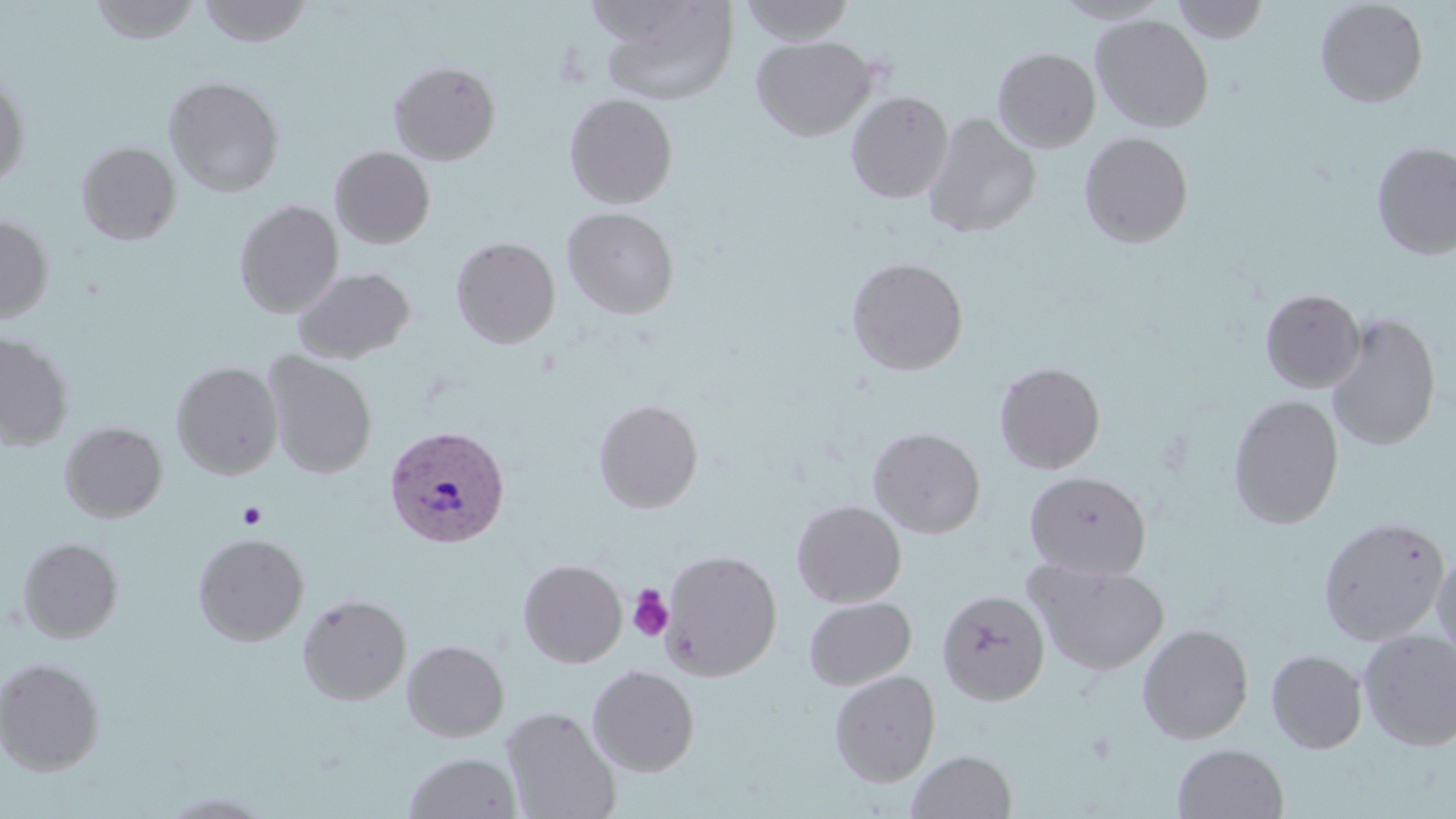

Summary:
  - Coordinate format: approximate bounding boxes as (x1, y1, x2, y2) in pixels
  - Platelet locations: (238, 501, 268, 528), (627, 584, 675, 642)
  - Plasmodium vivax-infected red blood cell locations: (383, 425, 511, 548)
  - Uninfected red blood cell locations: (89, 0, 202, 44), (198, 0, 313, 47), (739, 0, 857, 45), (1052, 0, 1173, 24), (1170, 0, 1271, 43), (1314, 0, 1428, 107), (593, 1, 739, 105), (1091, 14, 1214, 132), (751, 36, 878, 141), (992, 47, 1101, 153), (388, 60, 501, 165), (0, 74, 31, 192), (164, 76, 285, 197), (846, 91, 954, 203), (564, 92, 678, 209), (923, 112, 1042, 240), (1079, 131, 1194, 248), (76, 141, 181, 245), (1371, 141, 1456, 260), (329, 146, 435, 249), (234, 199, 344, 317), (562, 206, 680, 318), (0, 214, 54, 323), (450, 236, 561, 348), (846, 256, 968, 375), (291, 266, 416, 364), (1260, 288, 1367, 392), (1325, 312, 1442, 451), (0, 333, 75, 451), (263, 350, 378, 479), (171, 361, 284, 479), (994, 361, 1105, 474), (1228, 394, 1344, 529), (593, 398, 704, 513), (59, 421, 168, 523), (867, 426, 986, 538), (1024, 470, 1151, 579), (791, 499, 906, 608), (1317, 515, 1450, 646), (192, 532, 309, 646), (17, 536, 124, 642), (1431, 548, 1456, 669), (661, 549, 783, 680), (518, 558, 627, 668), (1024, 558, 1170, 676), (936, 589, 1049, 705), (298, 593, 412, 705), (804, 597, 917, 690), (1137, 624, 1254, 744), (1357, 629, 1456, 750), (402, 639, 510, 742), (1266, 649, 1368, 754), (0, 657, 105, 775), (587, 664, 700, 776), (829, 670, 941, 787), (501, 706, 621, 819), (1173, 743, 1289, 819), (905, 749, 1018, 819), (404, 751, 521, 819), (157, 791, 280, 818)
  - Slide-level diagnosis: Plasmodium vivax
  - Preparation: thin blood smear
  - Field of view: single
  - Magnification: 1000x
  - Stain: May-Grünwald-Giemsa
  - Image size: 1456×819 pixels
  - Modality: optical microscopy